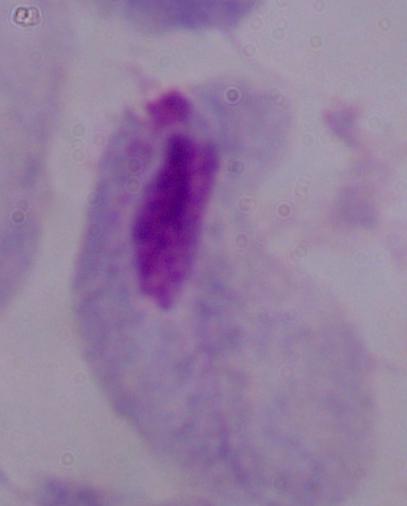

Photomicrograph. 1000x magnification. A trichomonad is seen.